Describe the morphology of the erythrocytes.
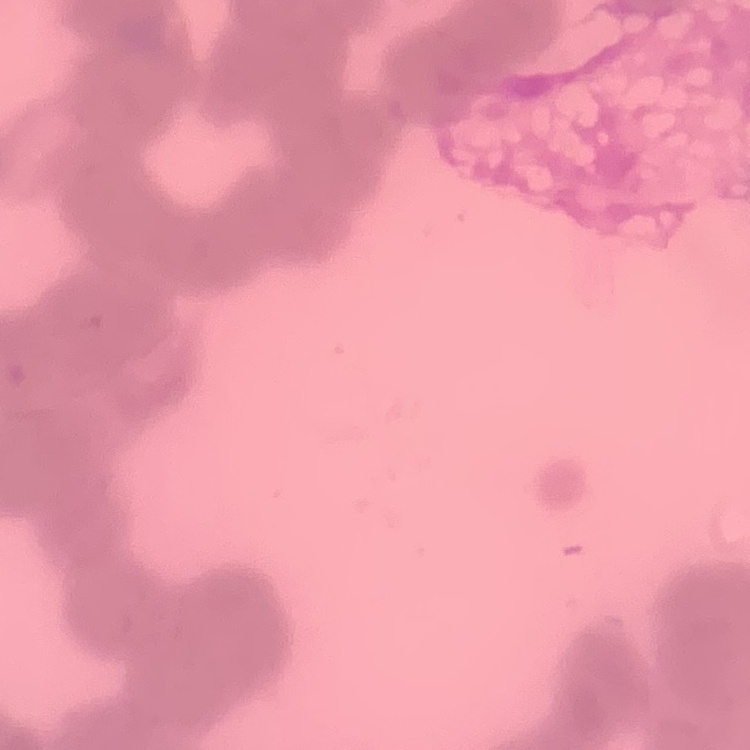

Rouleaux formation.

stain = Field's or Giemsa
preparation = thin blood film
image type = one tile cut from a larger photomicrograph